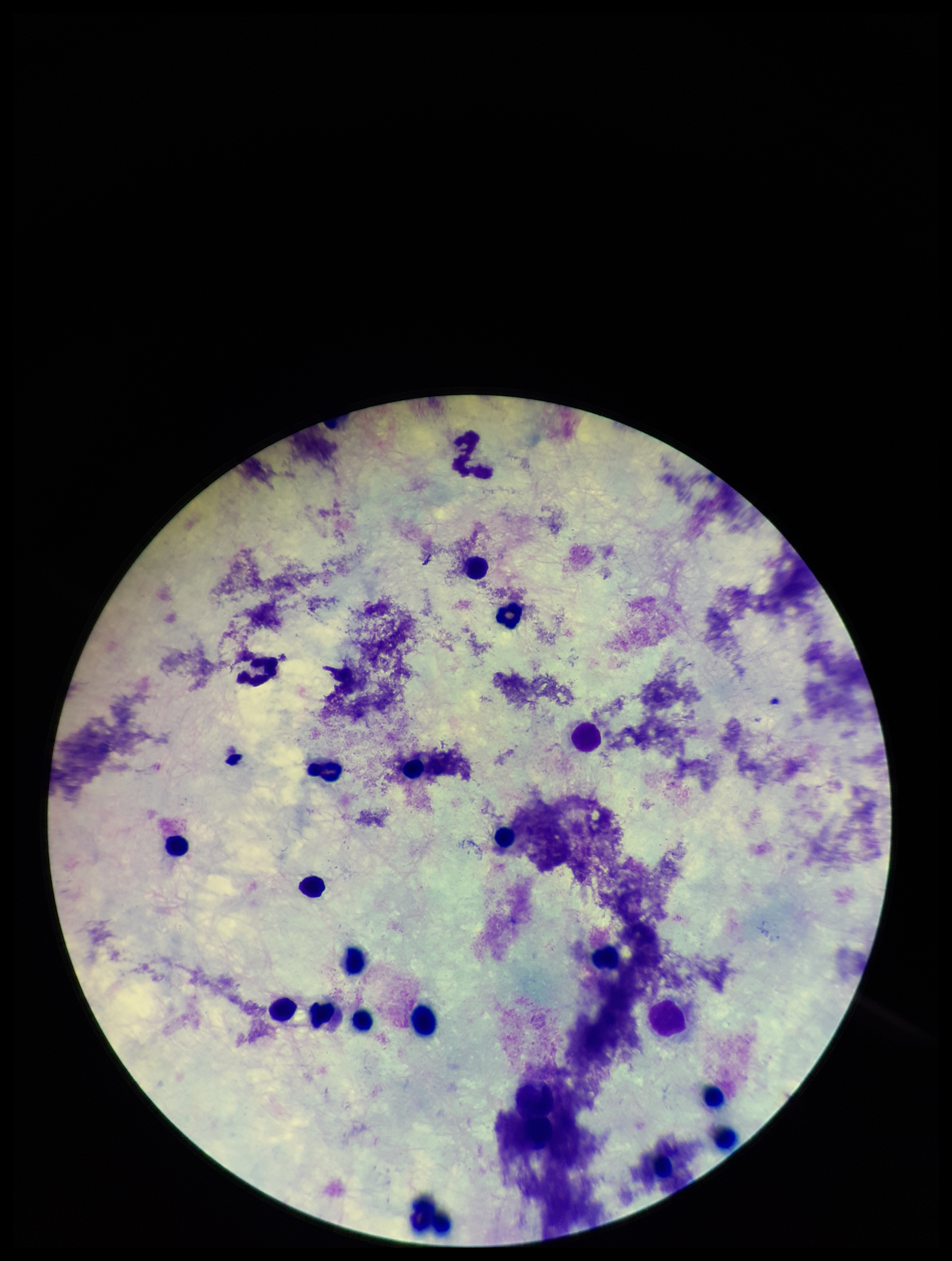

Summary:
  - Capture: smartphone photograph through the microscope eyepiece
  - Stain: Giemsa
  - Parasite count: 0
  - Leukocyte count: 20
  - Patient malaria status: negative
  - Plasmodium parasites: none seen
  - Image size: 952×1261 pixels
  - Field of view: single
  - Preparation: thick blood smear